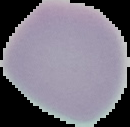

Malaria status: uninfected. From a thin blood film. Image is 130×127 pixels. Cell region segmented out of the field of view; the surrounding area is masked to black.